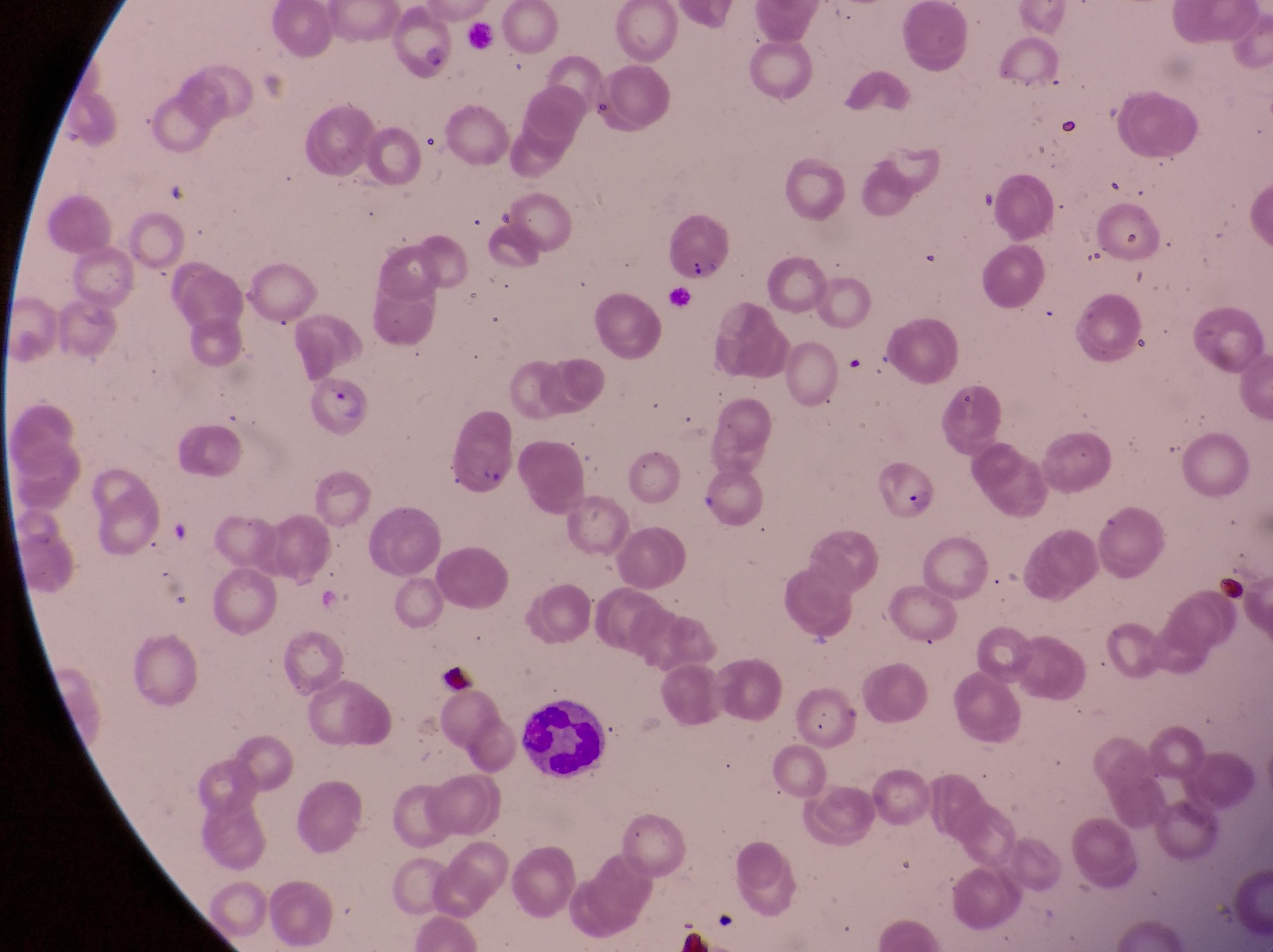
Approximate bounding boxes as {left, top, right, bottom} in pixels.
Summary:
  - Parasitised red blood cell locations: {385, 10, 463, 84}, {662, 210, 734, 284}, {310, 372, 372, 434}, {876, 440, 938, 525}
  - Artifact (platelet-like body, stain precipitate, or debris) locations: {1055, 116, 1076, 136}, {1220, 572, 1254, 608}, {435, 656, 474, 690}
  - Leukocyte locations: {519, 702, 604, 777}
  - Country: Uganda
  - Magnification: 1000x
  - Image size: 1273×952 pixels
  - Capture: smartphone photograph through the eyepiece of an Olympus CX-23 microscope
  - Field of view: single
  - Preparation: thin blood film